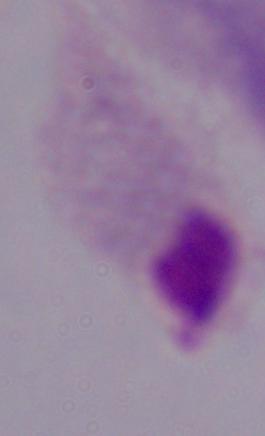
modality: photomicrograph
magnification: 1000x
identification: trichomonad